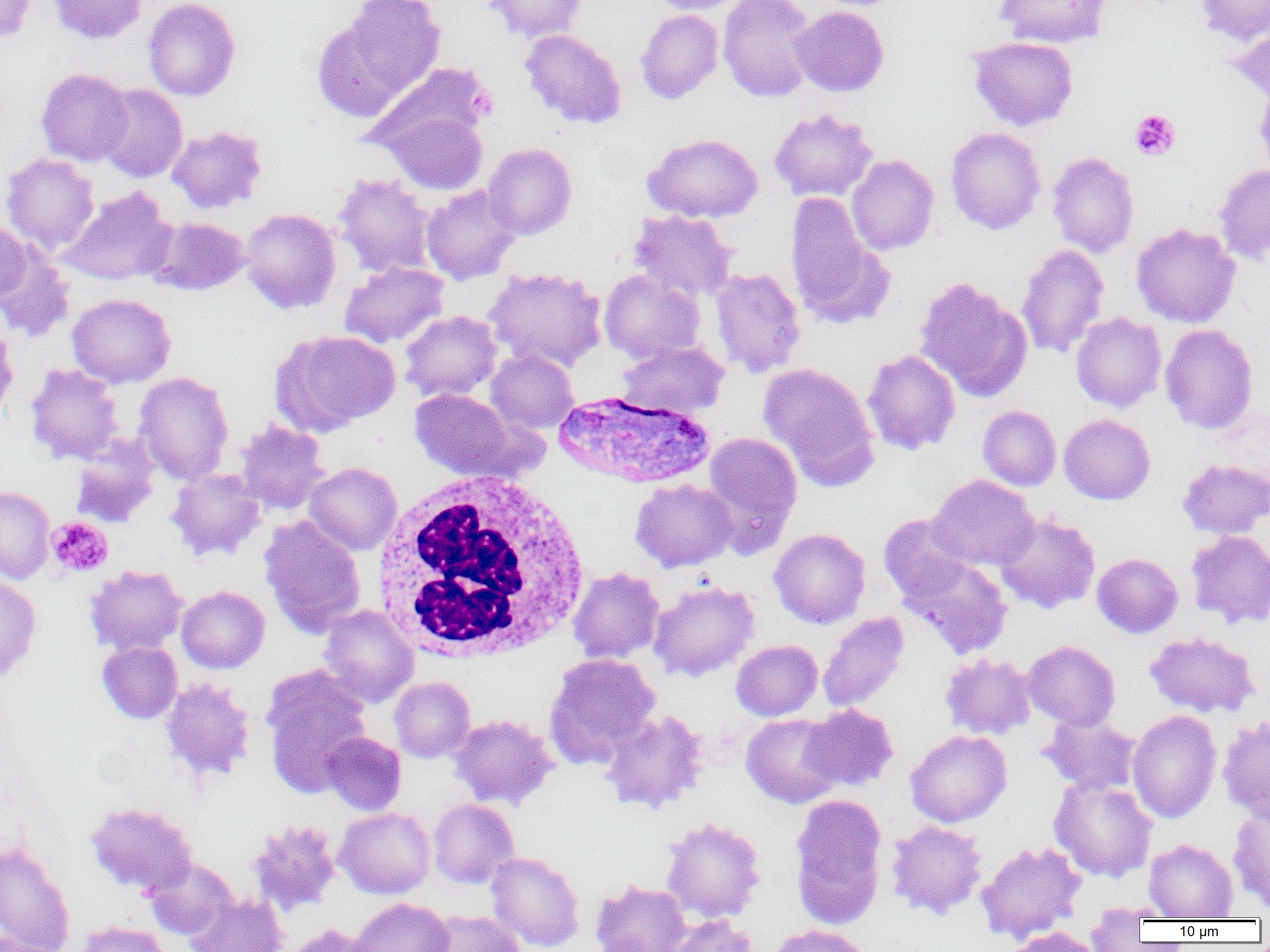

Summary:
  - Coordinate format: approximate bounding boxes as (x1,y1)-(x2,y2) corner pairs in pixels
  - Plasmodium vivax-infected red blood cell locations: (554,391)-(716,491)
  - White blood cell locations: (371,469)-(592,663)
  - Uninfected red blood cell locations: (0,0)-(35,44), (47,0)-(147,44), (143,0)-(241,101), (482,0)-(588,43), (644,0)-(747,14), (717,0)-(818,102), (993,0)-(1111,48), (1196,0)-(1270,45), (332,1)-(445,105), (790,5)-(889,97), (635,9)-(724,104), (1230,25)-(1270,108), (519,28)-(626,128), (967,36)-(1079,131), (363,62)-(495,160), (35,68)-(134,166), (97,84)-(188,182), (770,108)-(878,201), (383,109)-(487,195), (167,126)-(268,214), (945,127)-(1046,234), (643,133)-(763,223), (483,143)-(577,240), (1047,152)-(1139,258), (2,153)-(99,255), (846,154)-(939,255), (1214,163)-(1270,265), (23,166)-(145,270), (333,174)-(436,277), (422,184)-(521,284), (60,187)-(176,286), (785,192)-(888,327), (240,208)-(341,314), (629,210)-(739,301), (148,216)-(250,296), (0,220)-(32,305), (1131,223)-(1241,328), (1016,243)-(1109,359), (0,246)-(74,342), (339,262)-(449,348), (484,266)-(607,373), (709,267)-(806,378), (599,269)-(706,364), (915,277)-(1032,401), (67,293)-(176,388), (401,310)-(502,402), (1071,312)-(1167,412), (1160,323)-(1258,434), (0,324)-(18,425), (272,329)-(400,436), (617,339)-(729,417), (486,349)-(579,434), (862,349)-(961,455), (759,362)-(880,490), (25,363)-(125,465), (134,371)-(234,485), (409,388)-(518,480), (978,405)-(1061,491), (1059,414)-(1155,505), (234,420)-(330,514), (702,432)-(803,554), (69,438)-(160,529), (1178,458)-(1270,539), (304,462)-(402,555), (167,467)-(266,562), (928,474)-(1039,571), (630,478)-(738,573), (0,485)-(55,584), (994,512)-(1100,613), (878,514)-(971,603), (259,516)-(366,638), (769,528)-(870,628), (1186,530)-(1270,629), (1092,553)-(1183,638), (901,555)-(1013,659), (85,564)-(188,656), (567,566)-(665,664), (0,574)-(41,682), (648,579)-(760,682), (176,585)-(270,673), (318,604)-(419,707), (818,612)-(910,712), (1145,631)-(1261,718), (731,639)-(822,721), (1023,640)-(1120,730), (98,641)-(182,723), (940,652)-(1037,740), (543,653)-(661,769), (260,663)-(372,798), (389,676)-(475,763), (161,677)-(255,784), (802,704)-(898,791), (600,709)-(709,814), (1127,710)-(1222,823), (1040,713)-(1142,795), (449,714)-(558,810), (741,714)-(844,808), (1217,715)-(1270,824), (905,730)-(1012,827), (322,732)-(406,816), (1049,777)-(1158,882), (790,794)-(888,929), (428,799)-(519,889), (85,801)-(197,895), (1228,804)-(1270,911), (335,807)-(435,899), (660,816)-(766,923), (247,819)-(342,916), (886,820)-(988,918), (1144,838)-(1239,920), (0,841)-(76,952), (976,841)-(1086,943), (486,851)-(585,951), (144,857)-(238,940), (591,879)-(691,952), (187,893)-(289,952), (349,897)-(454,952), (1085,902)-(1176,922), (423,910)-(528,952), (1085,910)-(1154,950), (663,913)-(759,952), (74,920)-(172,952), (281,923)-(376,952), (766,924)-(873,952), (1000,927)-(1106,952), (1,931)-(65,952)
  - Platelet locations: (1130,109)-(1180,160), (47,516)-(113,578)
  - Slide-level diagnosis: Plasmodium vivax
  - Field of view: single
  - Image size: 1270×952 pixels
  - Magnification: 1000x
  - Preparation: thin blood smear
  - Modality: optical microscopy